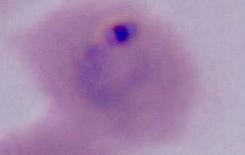
A Plasmodium parasite is seen. 400x or 1000x magnification. Micrograph.